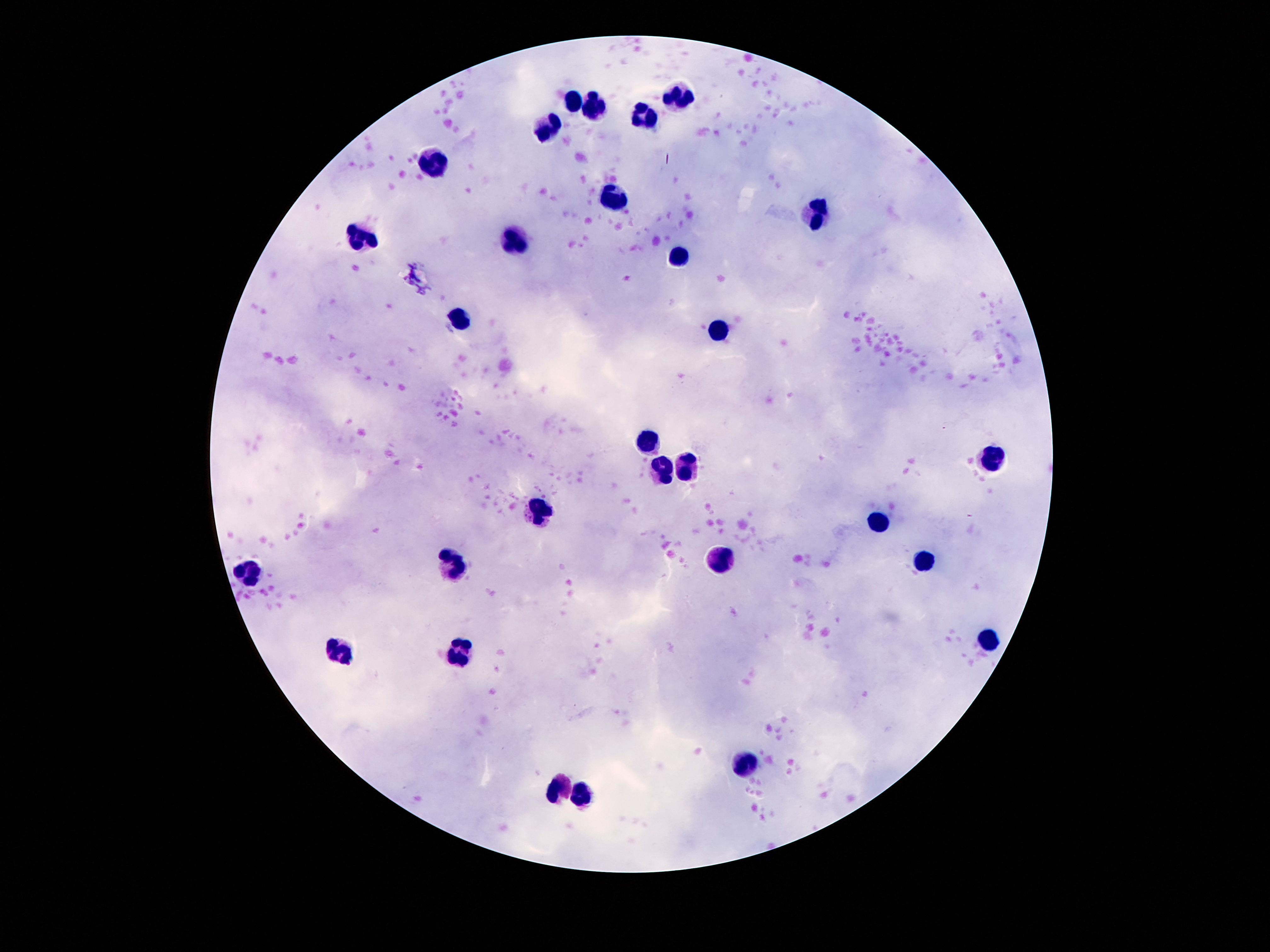
magnification = 100x
stain = Giemsa
field of view = one from this slide
patient malaria status = uninfected
image size = 1270×952 pixels
preparation = thick blood film
capture = smartphone camera through the microscope eyepiece
leukocyte locations = approximate centers as (x, y) in pixels: (576, 96), (677, 98), (595, 105), (643, 116), (552, 129), (434, 163), (614, 200), (813, 211), (363, 236), (517, 243), (683, 259), (459, 320), (720, 330), (651, 443), (989, 460), (688, 467), (662, 474), (537, 509), (875, 521), (922, 558), (722, 560), (455, 564), (246, 571), (989, 637), (335, 653), (464, 656), (748, 762), (558, 791), (580, 795)